Name the cell type shown.
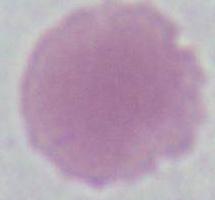
This is an erythrocyte.

modality = photomicrograph
magnification = 1000x